State which parasite is depicted.
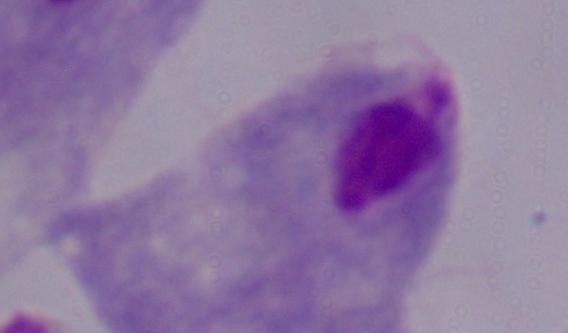

A trichomonad.

modality = photomicrograph
magnification = 1000x